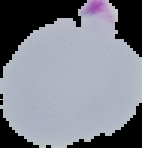

{
  "image_size": "142×148 pixels",
  "image_type": "segmented cell region with the area outside set to black",
  "preparation": "thin blood film",
  "malaria_status": "parasitized"
}